Locate every Plasmodium malariae-infected red blood cell.
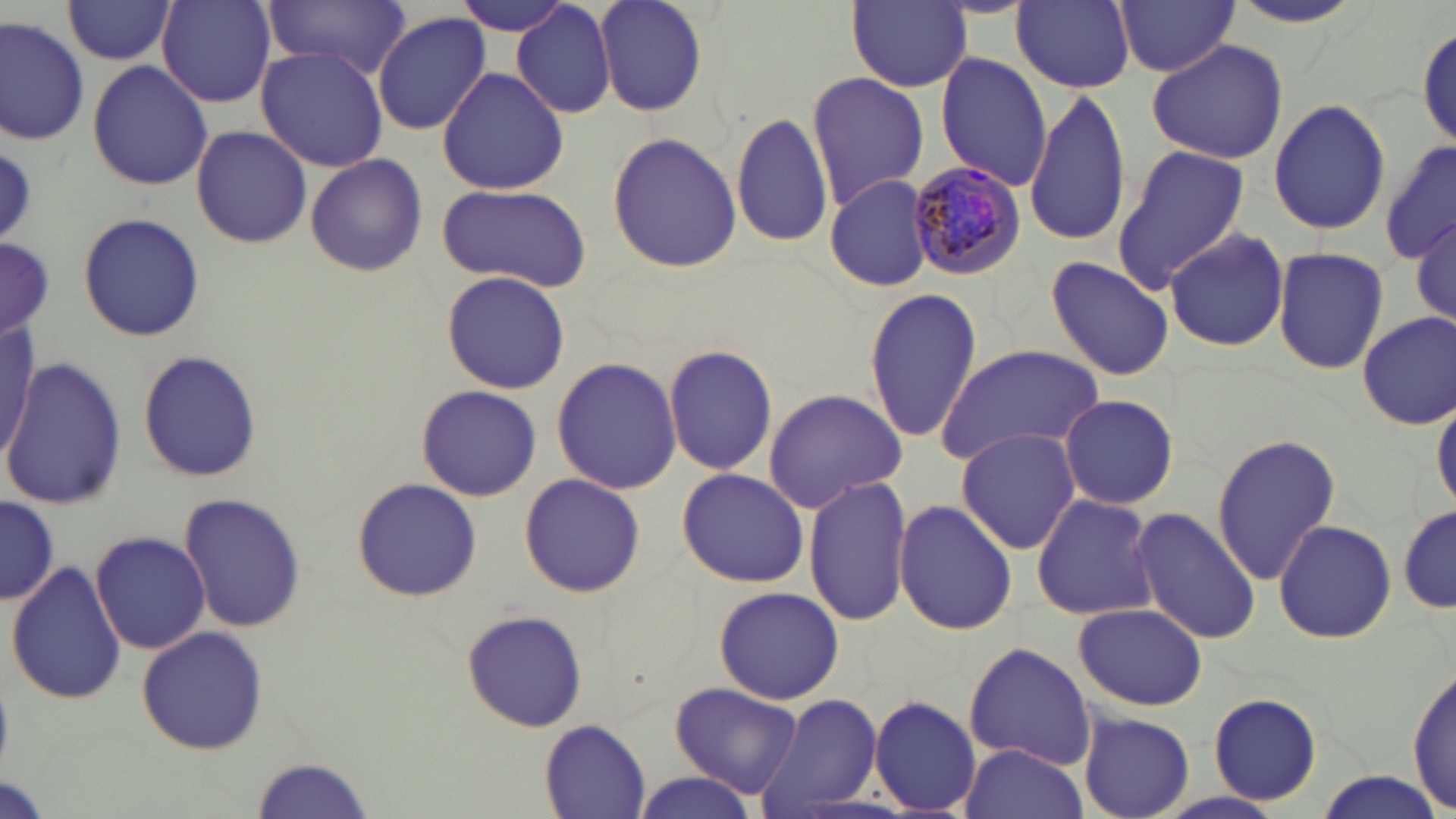
Approximate bounding boxes as named x1/y1/x2/y2 corners in pixels.
Plasmodium malariae-infected red blood cells: (x1=908, y1=157, x2=1027, y2=280).

Uninfected red blood cell locations: (x1=61, y1=0, x2=179, y2=65), (x1=157, y1=0, x2=276, y2=107), (x1=265, y1=0, x2=412, y2=77), (x1=456, y1=0, x2=577, y2=36), (x1=594, y1=0, x2=709, y2=117), (x1=1012, y1=0, x2=1136, y2=91), (x1=511, y1=1, x2=618, y2=119), (x1=844, y1=1, x2=973, y2=95), (x1=1113, y1=1, x2=1239, y2=76), (x1=372, y1=12, x2=489, y2=136), (x1=0, y1=17, x2=89, y2=144), (x1=1415, y1=23, x2=1454, y2=154), (x1=1146, y1=38, x2=1287, y2=165), (x1=254, y1=45, x2=390, y2=172), (x1=935, y1=53, x2=1052, y2=190), (x1=87, y1=61, x2=214, y2=191), (x1=437, y1=64, x2=569, y2=196), (x1=806, y1=71, x2=927, y2=210), (x1=1024, y1=93, x2=1132, y2=250), (x1=1269, y1=98, x2=1390, y2=235), (x1=731, y1=110, x2=832, y2=250), (x1=189, y1=125, x2=312, y2=249), (x1=607, y1=131, x2=741, y2=273), (x1=1380, y1=141, x2=1455, y2=269), (x1=1110, y1=145, x2=1248, y2=293), (x1=306, y1=154, x2=428, y2=277), (x1=821, y1=174, x2=936, y2=293), (x1=435, y1=184, x2=591, y2=293), (x1=78, y1=211, x2=204, y2=340), (x1=1412, y1=215, x2=1456, y2=331), (x1=1165, y1=228, x2=1290, y2=353), (x1=0, y1=235, x2=52, y2=342), (x1=1273, y1=246, x2=1389, y2=376), (x1=1044, y1=255, x2=1174, y2=382), (x1=440, y1=271, x2=570, y2=393), (x1=863, y1=288, x2=982, y2=444), (x1=1356, y1=310, x2=1456, y2=429), (x1=1, y1=318, x2=38, y2=461), (x1=664, y1=344, x2=777, y2=476), (x1=937, y1=344, x2=1105, y2=469), (x1=137, y1=349, x2=261, y2=482), (x1=552, y1=355, x2=683, y2=495), (x1=3, y1=360, x2=126, y2=509), (x1=414, y1=385, x2=542, y2=501), (x1=760, y1=387, x2=909, y2=513), (x1=1059, y1=394, x2=1178, y2=510), (x1=1432, y1=394, x2=1456, y2=515), (x1=956, y1=427, x2=1083, y2=554), (x1=1210, y1=433, x2=1341, y2=586), (x1=674, y1=468, x2=810, y2=587), (x1=519, y1=472, x2=646, y2=597), (x1=804, y1=476, x2=913, y2=624), (x1=352, y1=478, x2=482, y2=602), (x1=179, y1=491, x2=305, y2=635), (x1=1031, y1=493, x2=1160, y2=620), (x1=0, y1=496, x2=58, y2=604), (x1=892, y1=500, x2=1018, y2=635), (x1=1398, y1=504, x2=1455, y2=618), (x1=1131, y1=506, x2=1259, y2=645), (x1=1272, y1=518, x2=1396, y2=644), (x1=91, y1=531, x2=213, y2=654), (x1=6, y1=561, x2=126, y2=706), (x1=713, y1=586, x2=844, y2=705), (x1=1072, y1=602, x2=1207, y2=711), (x1=460, y1=611, x2=587, y2=731), (x1=136, y1=626, x2=268, y2=756), (x1=962, y1=641, x2=1098, y2=769), (x1=1408, y1=667, x2=1455, y2=814), (x1=669, y1=681, x2=804, y2=801), (x1=753, y1=692, x2=882, y2=817), (x1=1207, y1=693, x2=1321, y2=805), (x1=869, y1=696, x2=981, y2=815), (x1=1080, y1=712, x2=1194, y2=818), (x1=539, y1=718, x2=652, y2=818), (x1=959, y1=743, x2=1088, y2=819), (x1=249, y1=757, x2=376, y2=818), (x1=1308, y1=771, x2=1448, y2=818), (x1=633, y1=772, x2=761, y2=818), (x1=0, y1=777, x2=53, y2=819). Slide-level diagnosis: Plasmodium malariae. Light microscopy. Thin blood smear. May-Grünwald-Giemsa stain. Image is 1456×819 pixels. One field of a larger specimen. Captured at 1000x magnification.